Comment on the morphology of the erythrocytes.
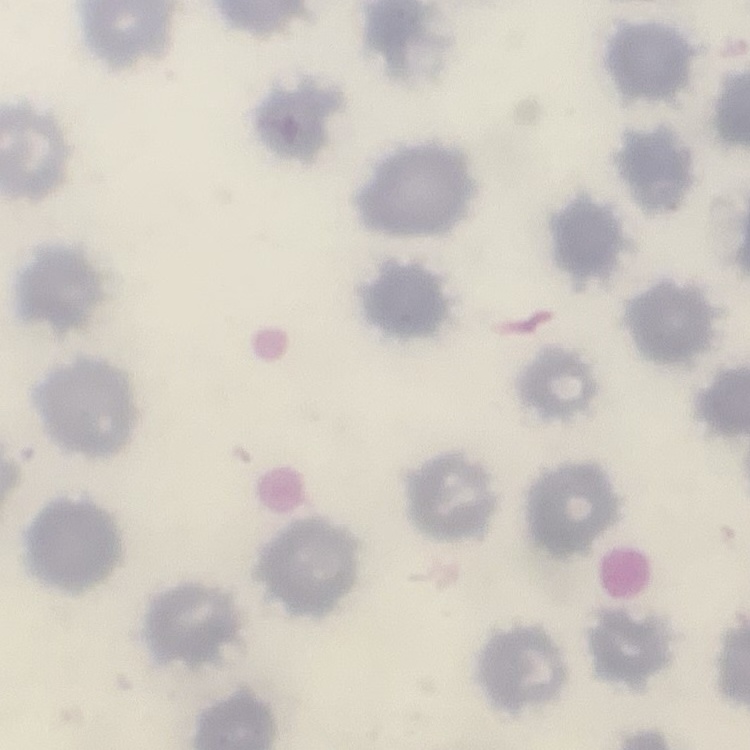
They show no rouleaux formation.

Summary:
  - Stain: Field's or Giemsa
  - Preparation: thin blood smear
  - Image type: one tile cut from a larger photomicrograph